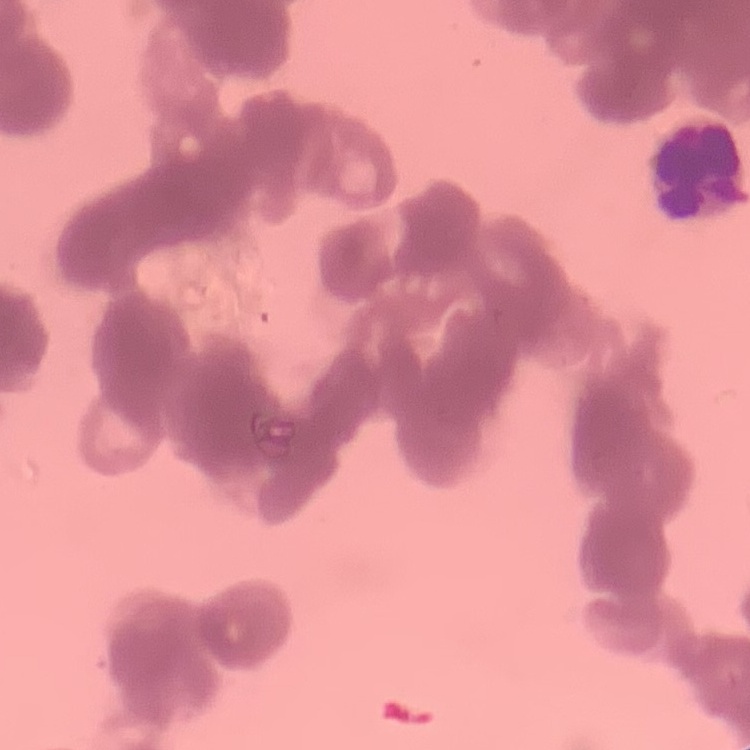

erythrocyte morphology = rouleaux formation
stain = Field's or Giemsa
image type = square crop of a larger photomicrograph
preparation = thin peripheral smear